Outline each blood parasite and name the species.
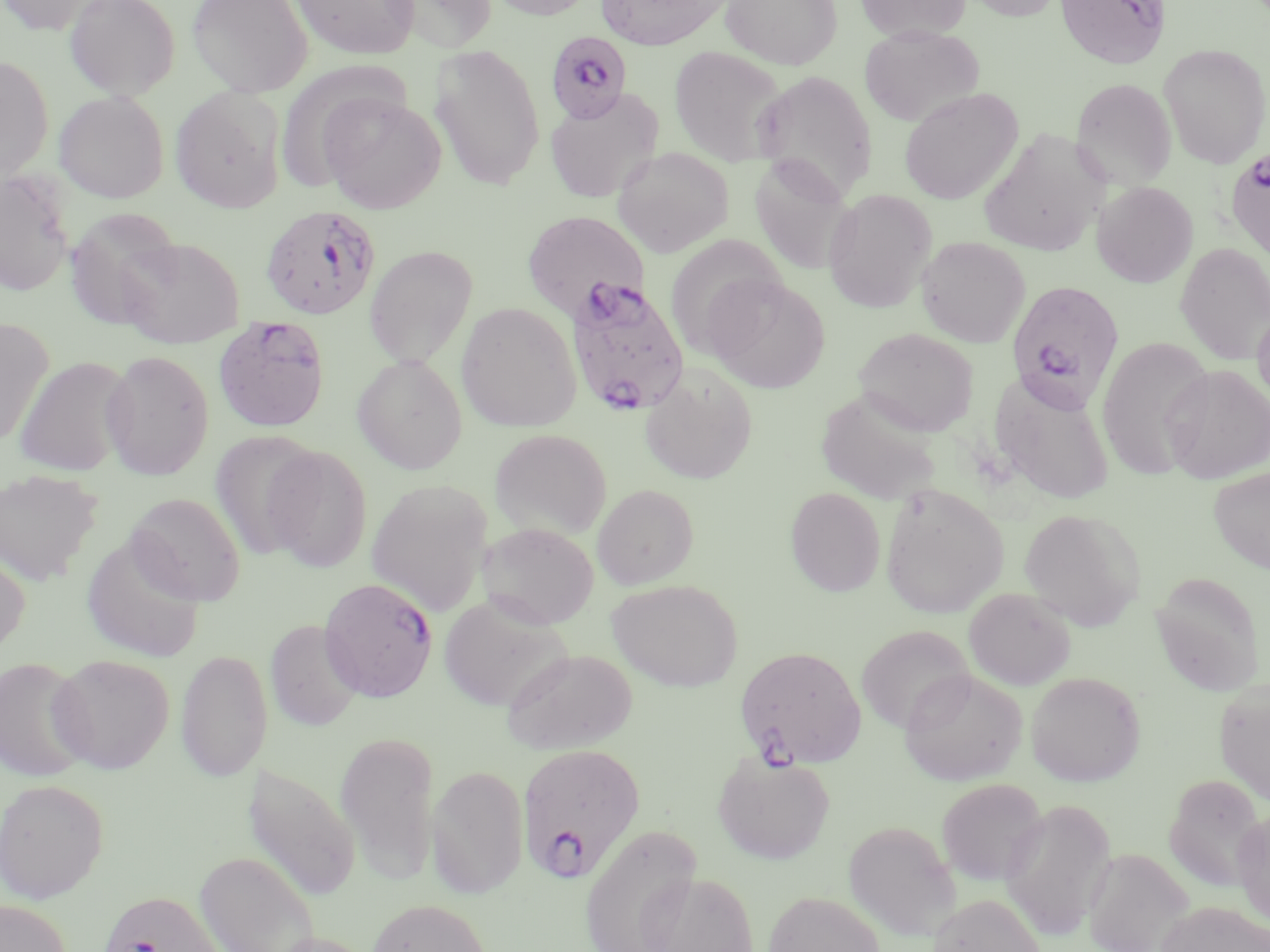

Approximate bounding boxes as (x1,y1)-(x2,y2) corner pairs in pixels.
Plasmodium falciparum-infected red blood cells: (1054,0)-(1170,69), (546,31)-(633,123), (1224,147)-(1270,264), (260,205)-(382,320), (563,276)-(691,417), (1008,281)-(1125,410), (213,316)-(330,432), (319,577)-(438,702), (734,645)-(867,769), (517,742)-(646,883), (96,890)-(228,952).
No Plasmodium ovale, Plasmodium malariae, Plasmodium vivax, Babesia divergens, or Trypanosoma brucei observed.

Summary:
  - Uninfected red blood cell locations: (0,0)-(110,36), (64,0)-(180,100), (187,0)-(312,98), (290,0)-(421,59), (391,0)-(498,53), (482,0)-(599,20), (596,0)-(732,50), (720,0)-(842,69), (856,0)-(972,41), (960,0)-(1066,21), (859,25)-(984,127), (1158,43)-(1270,168), (430,45)-(546,190), (668,45)-(788,166), (0,55)-(54,180), (750,69)-(878,203), (1071,77)-(1177,189), (170,87)-(287,213), (899,87)-(1022,205), (545,89)-(663,202), (54,90)-(169,203), (319,92)-(446,215), (977,130)-(1108,258), (612,147)-(734,257), (749,155)-(855,275), (0,171)-(75,297), (1092,181)-(1198,287), (823,189)-(937,313), (64,207)-(183,328), (522,211)-(650,320), (664,234)-(786,359), (916,236)-(1030,347), (115,237)-(245,348), (1175,242)-(1270,365), (365,245)-(478,369), (704,275)-(830,393), (456,301)-(581,432), (1252,302)-(1270,411), (0,316)-(54,447), (854,327)-(979,437), (1096,335)-(1214,480), (100,351)-(215,479), (14,355)-(135,476), (352,355)-(468,474), (640,363)-(757,485), (1161,365)-(1270,484), (990,372)-(1116,505), (813,387)-(945,508), (489,429)-(611,540), (209,430)-(323,559), (262,445)-(374,572), (1208,466)-(1270,574), (0,469)-(103,586), (366,479)-(493,615), (879,482)-(1009,619), (592,484)-(699,589), (785,487)-(886,597), (126,492)-(245,606), (1018,508)-(1145,630), (479,522)-(598,629), (81,532)-(207,663), (0,547)-(30,657), (1150,571)-(1265,697), (608,579)-(743,691), (963,587)-(1076,691), (438,596)-(571,712), (265,619)-(363,731), (857,625)-(973,733), (501,648)-(638,754), (176,649)-(272,782), (48,654)-(174,773), (0,657)-(93,783), (899,668)-(1028,786), (1026,671)-(1145,786), (1213,679)-(1270,805), (335,730)-(440,881), (713,752)-(835,865), (242,763)-(361,902), (426,764)-(529,899), (1165,773)-(1265,891), (0,778)-(108,903), (936,778)-(1049,887), (1000,796)-(1117,941), (1231,809)-(1270,928), (843,820)-(960,941), (579,824)-(702,952), (1082,847)-(1194,952), (194,850)-(319,952), (641,870)-(759,952), (764,891)-(885,952), (927,893)-(1046,952), (366,898)-(491,952), (0,899)-(70,952), (1156,901)-(1269,952), (264,931)-(375,952)
  - Slide-level diagnosis: Plasmodium falciparum
  - Preparation: thin blood smear
  - Stain: May-Grünwald-Giemsa
  - Modality: light microscopy
  - Field of view: single
  - Image size: 1270×952 pixels
  - Magnification: 1000x